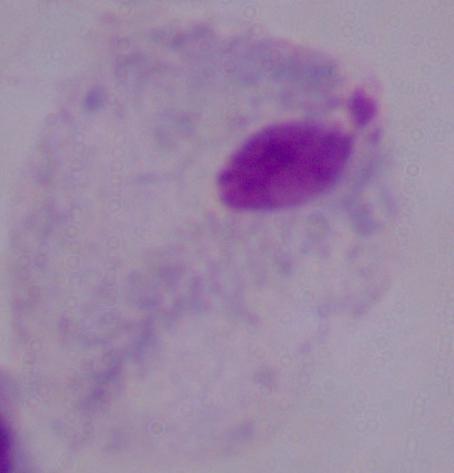

modality = micrograph
identification = trichomonad
magnification = 1000x